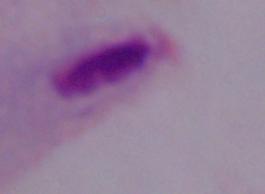

A trichomonad is shown. Captured at 1000x magnification. Photomicrograph.